Give the position of every malaria parasite.
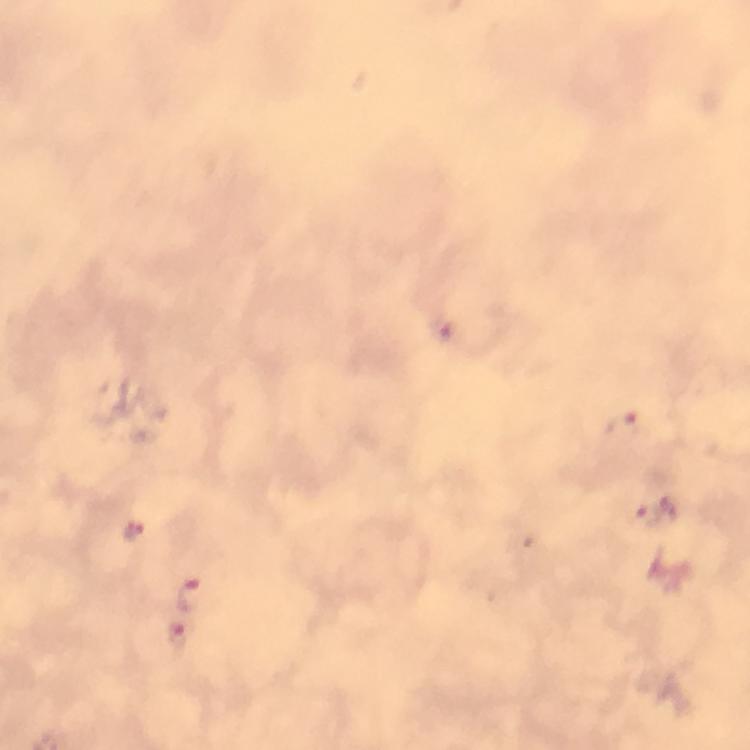
Approximate object centers, in pixels from the top-left corner.
Malaria parasites: (x=444, y=328), (x=627, y=424), (x=651, y=514), (x=133, y=532), (x=192, y=595), (x=180, y=638).

image size = 750×750 pixels
immersion oil = applied
capture = smartphone mounted on the microscope
stain = Giemsa
preparation = thick blood smear
magnification = 100x
context = from a malaria diagnostic workup
cropped from = one field of view